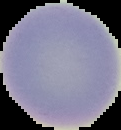
Cell region segmented out of the field of view; the surrounding area is masked to black. Result: negative for Plasmodium parasites. From a thin blood smear. Image is 121×130 pixels.